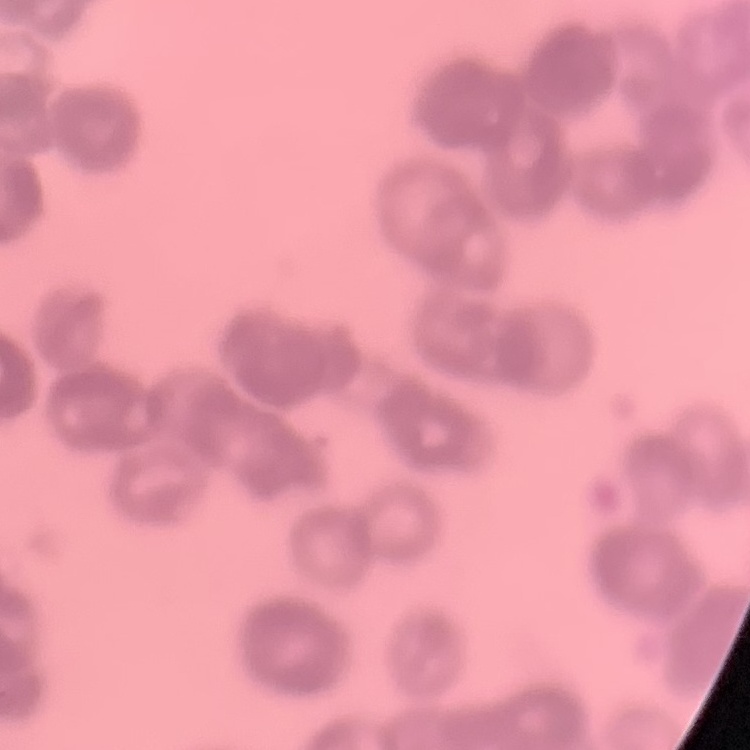
The erythrocytes exhibit rouleaux formation. Square crop of a larger photomicrograph. Field's or Giemsa stain. Thin blood film.